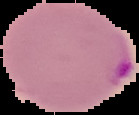 Image is 139×115 pixels. Cell region segmented out of the field of view; the surrounding area is masked to black. Result: Plasmodium parasites detected. From a thin blood smear.